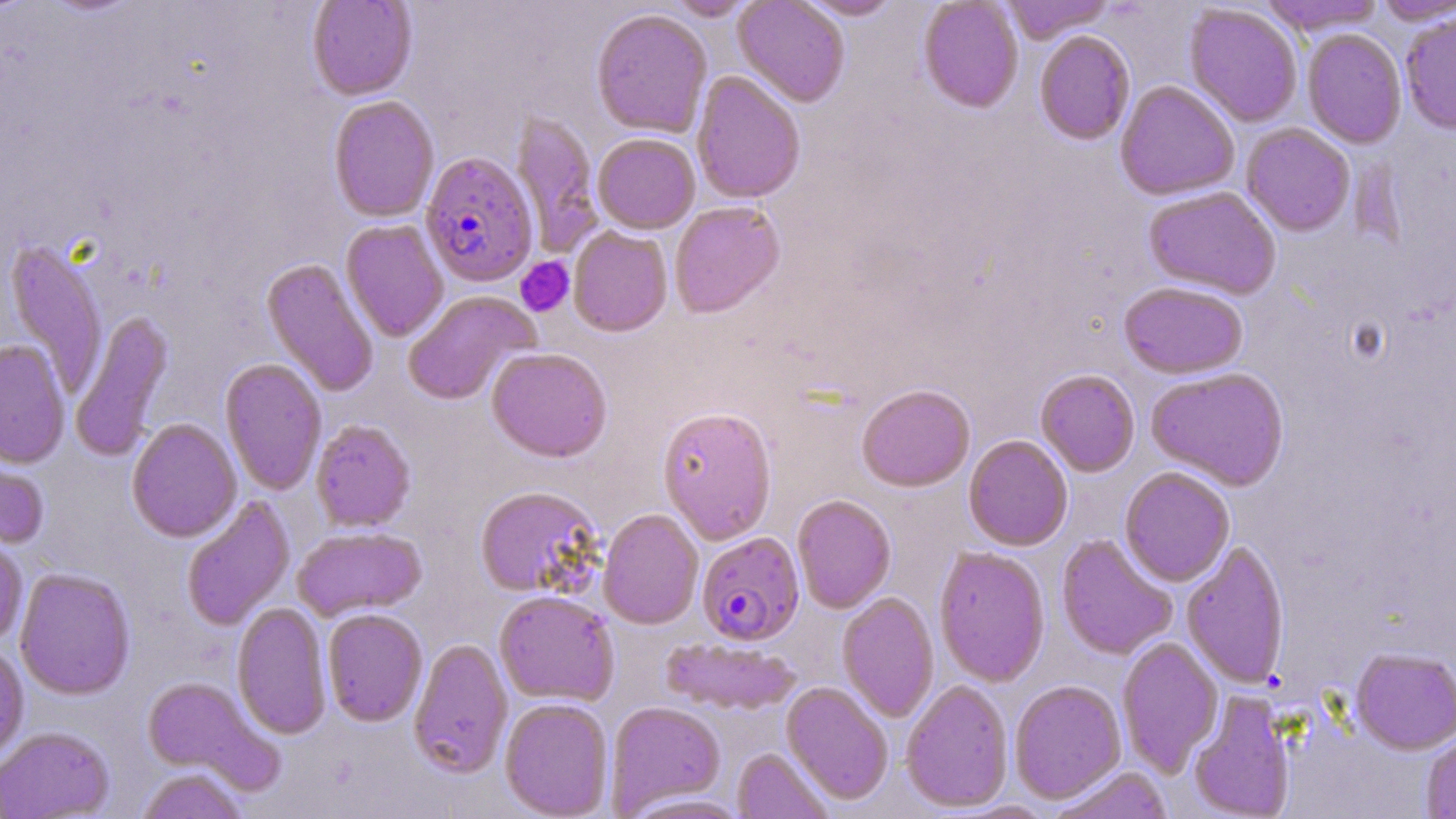

Summary:
  - Coordinate format: approximate bounding boxes as named x1/y1/x2/y2 corners in pixels
  - Platelet locations: (x1=515, y1=257, x2=574, y2=316)
  - Plasmodium falciparum-infected red blood cell locations: (x1=421, y1=153, x2=539, y2=289), (x1=696, y1=532, x2=804, y2=646)
  - Uninfected red blood cell locations: (x1=307, y1=0, x2=417, y2=101), (x1=666, y1=0, x2=759, y2=21), (x1=733, y1=0, x2=850, y2=107), (x1=798, y1=0, x2=903, y2=20), (x1=918, y1=0, x2=1024, y2=114), (x1=1001, y1=0, x2=1115, y2=44), (x1=1259, y1=0, x2=1388, y2=37), (x1=1373, y1=0, x2=1455, y2=26), (x1=1184, y1=5, x2=1302, y2=127), (x1=591, y1=9, x2=712, y2=138), (x1=1400, y1=13, x2=1456, y2=136), (x1=1302, y1=30, x2=1406, y2=149), (x1=1034, y1=31, x2=1135, y2=146), (x1=692, y1=72, x2=805, y2=205), (x1=1115, y1=81, x2=1240, y2=202), (x1=328, y1=96, x2=439, y2=223), (x1=510, y1=111, x2=604, y2=258), (x1=1241, y1=124, x2=1355, y2=236), (x1=593, y1=134, x2=700, y2=234), (x1=1143, y1=187, x2=1281, y2=300), (x1=669, y1=202, x2=784, y2=319), (x1=340, y1=220, x2=449, y2=343), (x1=568, y1=228, x2=673, y2=338), (x1=5, y1=239, x2=108, y2=397), (x1=261, y1=258, x2=379, y2=397), (x1=1118, y1=283, x2=1248, y2=380), (x1=403, y1=290, x2=541, y2=405), (x1=69, y1=309, x2=174, y2=462), (x1=0, y1=341, x2=70, y2=468), (x1=486, y1=348, x2=612, y2=464), (x1=220, y1=359, x2=327, y2=495), (x1=1146, y1=368, x2=1290, y2=491), (x1=1035, y1=370, x2=1140, y2=477), (x1=857, y1=384, x2=975, y2=492), (x1=658, y1=408, x2=777, y2=545), (x1=127, y1=418, x2=242, y2=543), (x1=310, y1=420, x2=415, y2=532), (x1=963, y1=435, x2=1073, y2=551), (x1=0, y1=440, x2=50, y2=550), (x1=1120, y1=468, x2=1235, y2=586), (x1=475, y1=486, x2=603, y2=598), (x1=181, y1=495, x2=296, y2=632), (x1=792, y1=495, x2=896, y2=614), (x1=598, y1=509, x2=703, y2=629), (x1=292, y1=527, x2=427, y2=621), (x1=1056, y1=534, x2=1178, y2=661), (x1=0, y1=537, x2=28, y2=647), (x1=1181, y1=542, x2=1291, y2=689), (x1=933, y1=544, x2=1177, y2=672), (x1=934, y1=546, x2=1050, y2=687), (x1=15, y1=568, x2=136, y2=700), (x1=494, y1=591, x2=619, y2=706), (x1=837, y1=593, x2=939, y2=723), (x1=232, y1=602, x2=331, y2=739), (x1=322, y1=608, x2=428, y2=727), (x1=1117, y1=636, x2=1224, y2=777), (x1=661, y1=637, x2=802, y2=715), (x1=408, y1=639, x2=513, y2=779), (x1=0, y1=644, x2=29, y2=765), (x1=1350, y1=647, x2=1456, y2=756), (x1=141, y1=676, x2=276, y2=788), (x1=901, y1=680, x2=1013, y2=812), (x1=1009, y1=680, x2=1127, y2=805), (x1=780, y1=681, x2=894, y2=805), (x1=1187, y1=690, x2=1296, y2=819), (x1=500, y1=698, x2=614, y2=818), (x1=606, y1=701, x2=725, y2=815), (x1=0, y1=726, x2=114, y2=818), (x1=1421, y1=733, x2=1456, y2=818), (x1=732, y1=748, x2=832, y2=819), (x1=135, y1=767, x2=248, y2=819), (x1=1049, y1=767, x2=1173, y2=819), (x1=622, y1=793, x2=753, y2=819)
  - Slide-level diagnosis: Plasmodium falciparum
  - Modality: optical microscopy
  - Field of view: one of a larger specimen
  - Preparation: thin blood smear
  - Stain: May-Grünwald-Giemsa
  - Image size: 1456×819 pixels
  - Magnification: 1000x